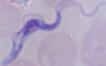 1000x magnification. Photomicrograph. A trypanosome is shown.